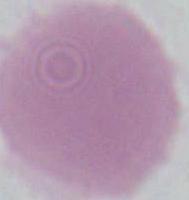
modality = micrograph
magnification = 1000x
identification = erythrocyte